Identify the parasite.
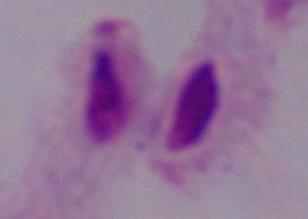
This is a trichomonad.

modality = micrograph
magnification = 1000x